Name the parasite shown.
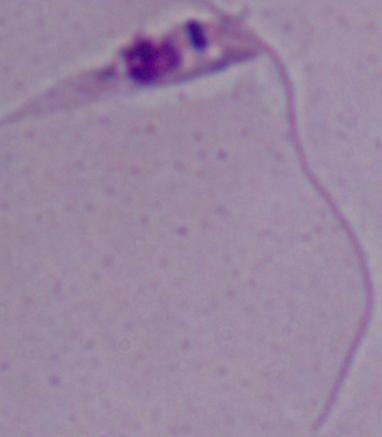
This is Leishmania.

Micrograph. Captured at 1000x magnification.